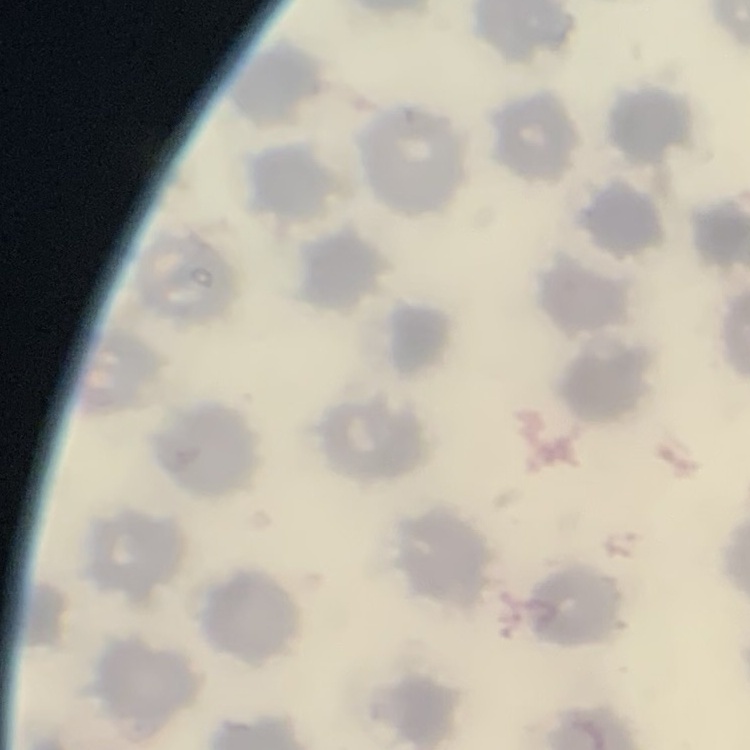

erythrocyte_morphology: no rouleaux formation
stain: Field's or Giemsa
preparation: thin peripheral smear
image_type: one tile cut from a larger photomicrograph